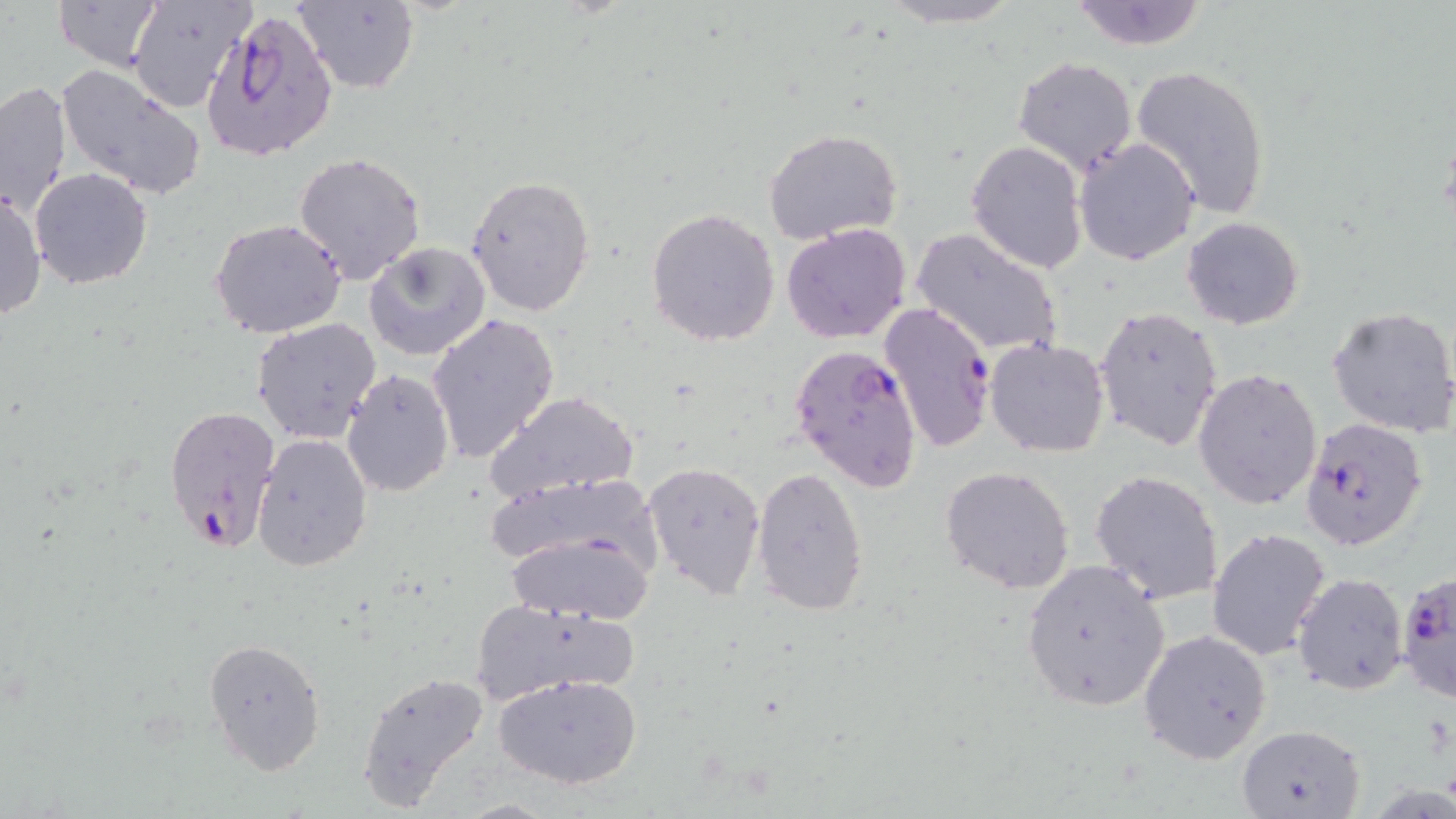

Approximate bounding boxes as named x1/y1/x2/y2 corners in pixels. Plasmodium falciparum-infected red blood cell locations: (x1=203, y1=12, x2=337, y2=159), (x1=879, y1=303, x2=997, y2=454), (x1=790, y1=344, x2=924, y2=493), (x1=162, y1=405, x2=281, y2=557), (x1=1302, y1=416, x2=1431, y2=551), (x1=1397, y1=571, x2=1456, y2=703). Uninfected red blood cell locations: (x1=50, y1=0, x2=168, y2=73), (x1=130, y1=0, x2=256, y2=112), (x1=292, y1=0, x2=419, y2=94), (x1=874, y1=0, x2=1026, y2=28), (x1=1067, y1=0, x2=1210, y2=50), (x1=1012, y1=57, x2=1138, y2=175), (x1=1129, y1=64, x2=1273, y2=220), (x1=56, y1=65, x2=208, y2=200), (x1=0, y1=81, x2=71, y2=217), (x1=763, y1=129, x2=903, y2=245), (x1=1074, y1=137, x2=1201, y2=265), (x1=965, y1=141, x2=1087, y2=272), (x1=292, y1=153, x2=427, y2=285), (x1=29, y1=168, x2=152, y2=289), (x1=467, y1=174, x2=597, y2=318), (x1=0, y1=185, x2=47, y2=325), (x1=647, y1=206, x2=780, y2=346), (x1=1181, y1=216, x2=1304, y2=330), (x1=209, y1=217, x2=349, y2=340), (x1=781, y1=223, x2=912, y2=345), (x1=910, y1=226, x2=1066, y2=360), (x1=363, y1=242, x2=491, y2=361), (x1=1328, y1=304, x2=1456, y2=437), (x1=1094, y1=307, x2=1222, y2=452), (x1=427, y1=313, x2=560, y2=464), (x1=251, y1=318, x2=383, y2=444), (x1=985, y1=338, x2=1111, y2=458), (x1=339, y1=367, x2=454, y2=499), (x1=1195, y1=367, x2=1324, y2=510), (x1=483, y1=391, x2=640, y2=508), (x1=250, y1=434, x2=373, y2=573), (x1=643, y1=459, x2=766, y2=599), (x1=939, y1=465, x2=1076, y2=594), (x1=750, y1=466, x2=871, y2=617), (x1=1090, y1=470, x2=1224, y2=605), (x1=483, y1=473, x2=664, y2=579), (x1=1206, y1=527, x2=1330, y2=663), (x1=501, y1=529, x2=657, y2=624), (x1=1021, y1=559, x2=1172, y2=712), (x1=1292, y1=571, x2=1409, y2=696), (x1=467, y1=597, x2=636, y2=707), (x1=1139, y1=630, x2=1273, y2=764), (x1=203, y1=636, x2=327, y2=774), (x1=356, y1=669, x2=492, y2=813), (x1=494, y1=674, x2=643, y2=789), (x1=1235, y1=723, x2=1365, y2=818). Slide-level diagnosis: Plasmodium falciparum. Thin blood film. May-Grünwald-Giemsa-stained preparation. 1000x magnification. Light microscopy. Single field of view. Image is 1456×819 pixels.